Identify the cell.
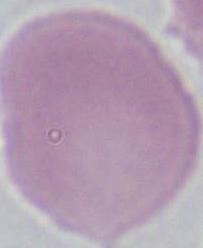

This is an erythrocyte.

magnification = 1000x
modality = micrograph